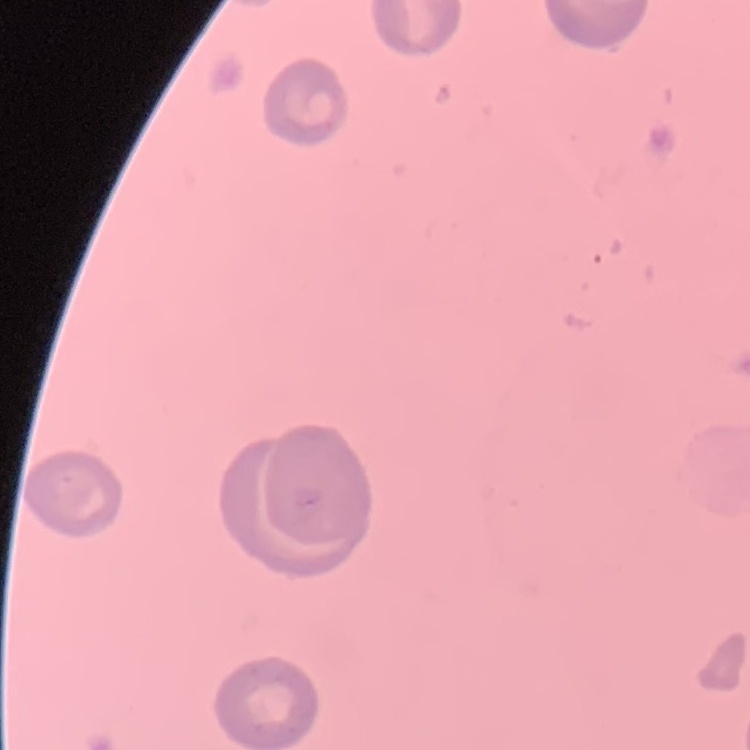
erythrocyte_morphology: no rouleaux formation
stain: Field's or Giemsa
preparation: thin blood film
image_type: one tile cut from a larger photomicrograph